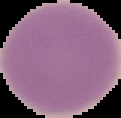 The area outside the segmented cell region is set to black. Image is 121×118 pixels. Result: negative for malaria parasites. From a thin blood film.